State which parasite is depicted.
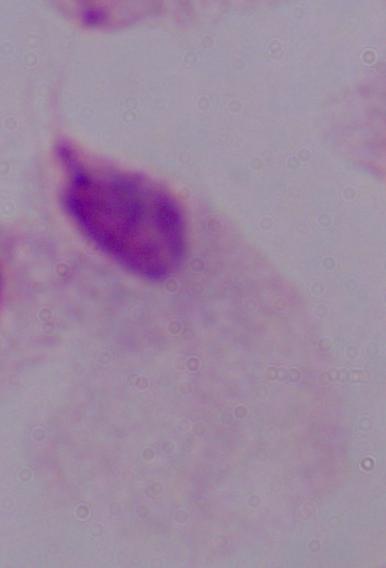
A trichomonad.

modality = photomicrograph
magnification = 1000x